Assess for parasitized red blood cells.
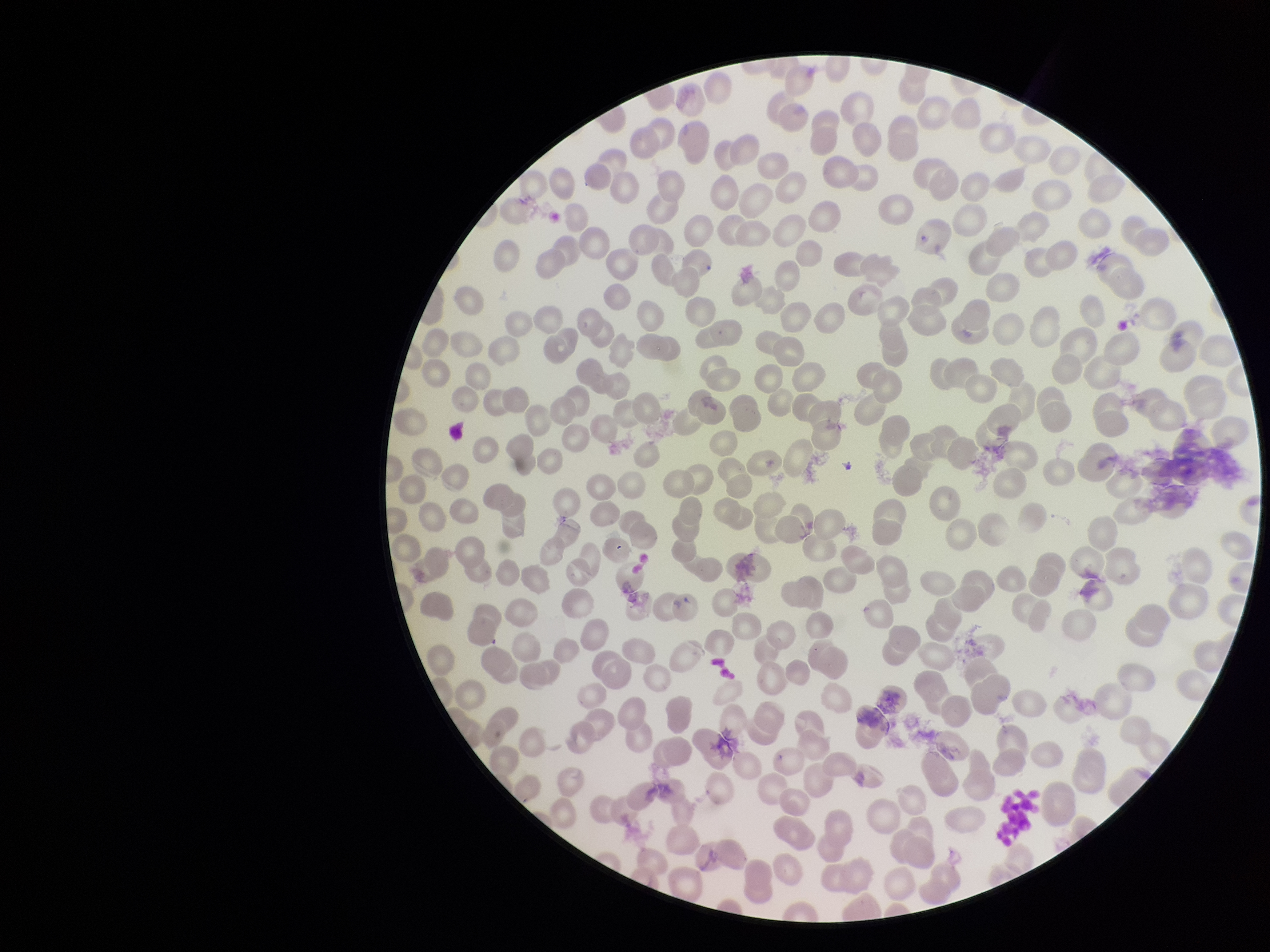
None detected.

{
  "red_blood_cell_count": 230,
  "field_of_view": "single",
  "stain": "Giemsa",
  "preparation": "thin smear",
  "image_size": "1270×952 pixels",
  "patient_malaria_status": "negative",
  "parasitized_red_blood_cell_count": 0,
  "capture": "smartphone photograph through the microscope eyepiece"
}